Give the extent of all Plasmodium malariae-infected red blood cells.
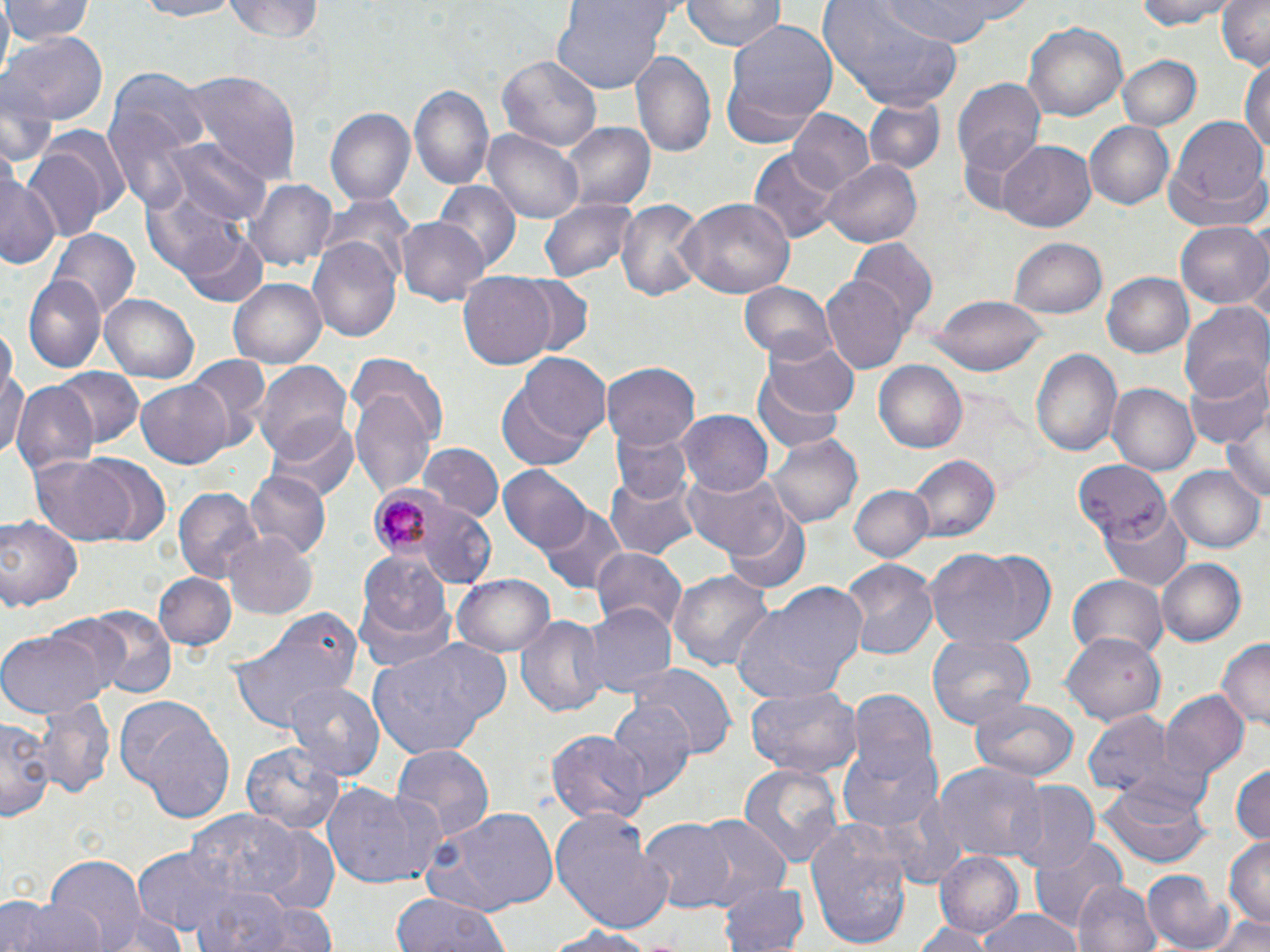
Approximate bounding boxes as [x1, y1, x2, y2] in pixels.
Plasmodium malariae-infected red blood cells: [367, 485, 450, 562].

Uninfected red blood cell locations: [4, 0, 93, 47], [125, 0, 246, 21], [681, 0, 786, 53], [875, 0, 1012, 43], [1134, 0, 1234, 31], [1214, 0, 1270, 69], [226, 1, 328, 43], [550, 1, 672, 95], [818, 2, 969, 111], [721, 21, 839, 146], [1022, 21, 1128, 125], [2, 31, 107, 128], [632, 47, 718, 163], [1117, 55, 1201, 132], [499, 56, 600, 153], [1242, 56, 1270, 162], [105, 65, 209, 204], [175, 68, 303, 181], [954, 75, 1046, 190], [410, 82, 495, 193], [864, 98, 946, 175], [326, 107, 415, 208], [786, 110, 876, 197], [1168, 116, 1268, 213], [1087, 121, 1175, 211], [564, 124, 655, 213], [485, 128, 584, 223], [165, 138, 269, 226], [23, 140, 115, 240], [997, 141, 1097, 233], [751, 148, 841, 245], [822, 158, 922, 248], [1163, 164, 1270, 237], [0, 167, 60, 274], [241, 177, 336, 272], [139, 183, 255, 285], [435, 183, 521, 274], [615, 197, 706, 305], [679, 197, 796, 303], [540, 198, 641, 283], [396, 216, 490, 304], [1177, 222, 1270, 308], [184, 228, 270, 308], [53, 229, 137, 319], [309, 236, 402, 343], [1008, 237, 1107, 317], [849, 240, 939, 329], [1102, 271, 1194, 358], [458, 272, 558, 368], [26, 273, 108, 373], [822, 277, 908, 375], [229, 278, 326, 370], [738, 281, 835, 365], [100, 293, 199, 382], [929, 295, 1050, 376], [1180, 300, 1270, 402], [765, 338, 860, 421], [0, 345, 29, 468], [1030, 348, 1122, 457], [185, 356, 270, 445], [749, 359, 854, 454], [254, 360, 353, 463], [496, 360, 607, 469], [603, 360, 702, 450], [874, 360, 971, 452], [1185, 364, 1270, 450], [54, 367, 144, 449], [349, 378, 439, 500], [135, 379, 235, 468], [10, 381, 98, 477], [1107, 383, 1198, 475], [678, 410, 773, 496], [1222, 411, 1270, 505], [266, 415, 358, 502], [614, 428, 691, 508], [767, 435, 862, 529], [419, 444, 501, 522], [29, 453, 140, 547], [75, 454, 171, 545], [908, 455, 1000, 542], [1072, 459, 1169, 542], [499, 466, 590, 555], [1168, 467, 1264, 553], [684, 470, 791, 560], [245, 472, 331, 557], [605, 476, 700, 559], [849, 484, 934, 561], [172, 486, 259, 585], [722, 501, 812, 595], [416, 505, 498, 587], [539, 505, 628, 595], [1100, 505, 1192, 591], [0, 514, 82, 614], [223, 530, 316, 620], [927, 546, 1058, 651], [591, 547, 687, 635], [358, 553, 453, 641], [1155, 555, 1246, 644], [841, 558, 940, 659], [668, 569, 774, 675], [153, 572, 238, 653], [1067, 573, 1169, 662], [451, 575, 555, 657], [354, 583, 456, 678], [732, 585, 869, 701], [578, 600, 676, 696], [78, 607, 177, 696], [226, 607, 362, 735], [515, 613, 608, 718], [0, 630, 110, 718], [1061, 631, 1168, 726], [927, 633, 1036, 731], [366, 638, 512, 760], [1216, 638, 1270, 732], [630, 665, 737, 757], [283, 680, 386, 781], [745, 686, 862, 779], [1158, 690, 1249, 784], [847, 691, 941, 789], [18, 697, 115, 802], [967, 699, 1079, 784], [607, 700, 696, 799], [118, 702, 235, 821], [1082, 711, 1176, 798], [1, 713, 53, 823], [548, 726, 650, 824], [241, 739, 343, 838], [390, 742, 494, 845], [837, 743, 944, 836], [933, 759, 1044, 864], [1230, 762, 1269, 848], [737, 763, 846, 871], [1008, 782, 1100, 875], [1096, 783, 1212, 869], [323, 784, 441, 889], [426, 806, 560, 915], [184, 809, 309, 903], [550, 809, 673, 932], [691, 817, 789, 902], [805, 818, 915, 951], [638, 819, 736, 911], [1027, 835, 1127, 933], [1224, 838, 1269, 928], [129, 847, 240, 935], [934, 851, 1024, 938], [41, 854, 150, 948], [1142, 866, 1233, 951], [715, 880, 809, 952], [1073, 881, 1162, 952], [188, 886, 329, 952], [391, 893, 511, 952], [7, 895, 105, 952], [87, 906, 194, 952], [975, 910, 1085, 952], [1204, 912, 1270, 951], [910, 921, 993, 952], [536, 923, 662, 951]. Slide-level diagnosis: Plasmodium malariae. Light microscopy. Image is 1270×952 pixels. Thin blood smear. May-Grünwald-Giemsa-stained preparation. One field of a larger specimen. 1000x magnification.